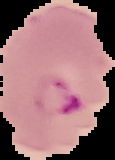
Summary:
  - Image type: segmented cell region on a black background
  - Malaria status: parasitized
  - Preparation: thin blood film
  - Image size: 115×160 pixels